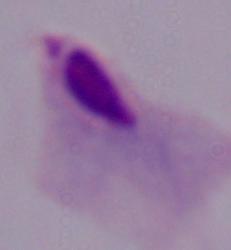
A trichomonad is shown. Micrograph. Captured at 1000x magnification.